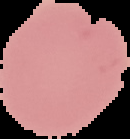 Segmented cell region on a black background. Malaria status: uninfected. Image is 130×139 pixels. From a thin blood film.